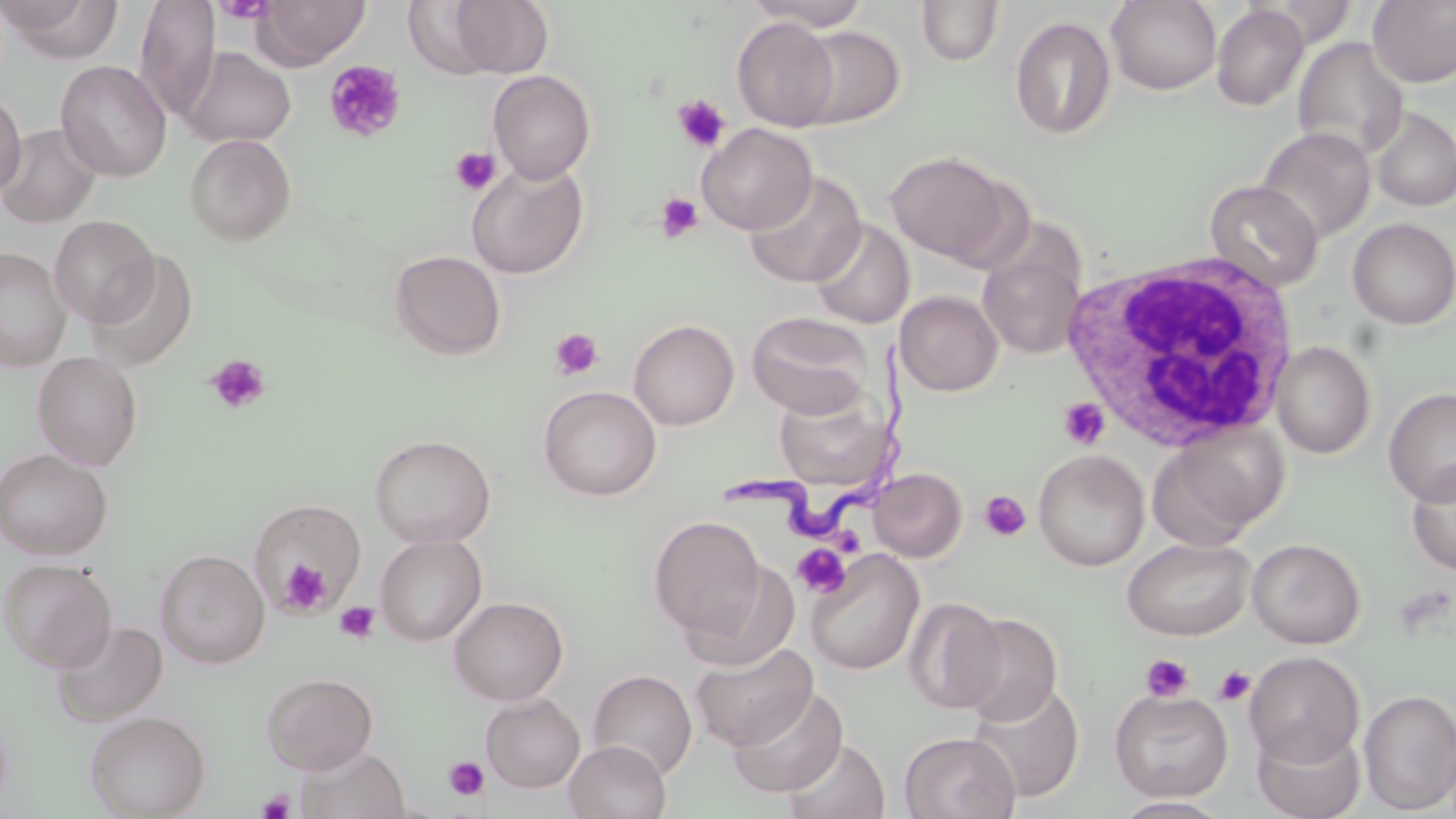
Approximate bounding boxes as (x1,y1)-(x2,y2) corner pairs in pixels. Platelet locations: (216,0)-(275,23), (324,60)-(406,143), (672,94)-(731,153), (449,146)-(501,195), (655,192)-(703,243), (548,328)-(604,381), (205,354)-(272,415), (1058,398)-(1110,450), (980,490)-(1031,541), (792,544)-(851,599), (280,561)-(331,611), (334,600)-(379,644), (1141,654)-(1194,702), (1213,665)-(1256,706), (443,756)-(490,801), (257,788)-(295,818). Trypanosoma brucei locations: (724,337)-(921,545). White blood cell locations: (1062,251)-(1303,454). Uninfected red blood cell locations: (2,0)-(123,61), (134,0)-(220,121), (252,0)-(371,69), (744,0)-(873,31), (1368,0)-(1456,87), (447,1)-(554,76), (916,1)-(1004,66), (1106,1)-(1221,95), (1210,3)-(1309,111), (1009,10)-(1219,118), (1010,16)-(1116,140), (732,17)-(840,131), (791,25)-(905,128), (1292,36)-(1409,161), (180,46)-(296,148), (56,60)-(171,181), (488,70)-(596,183), (0,89)-(26,198), (1371,107)-(1456,211), (0,123)-(101,228), (697,123)-(817,235), (1256,127)-(1376,243), (185,133)-(297,246), (885,151)-(1013,264), (466,160)-(589,279), (745,172)-(866,288), (1204,180)-(1323,292), (49,215)-(159,327), (1347,217)-(1456,329), (808,219)-(914,329), (0,247)-(71,371), (978,248)-(1085,360), (390,250)-(506,360), (84,252)-(199,371), (895,290)-(1003,396), (746,312)-(874,418), (628,318)-(740,430), (1271,340)-(1376,459), (32,350)-(143,470), (538,385)-(661,501), (1383,387)-(1456,505), (773,392)-(892,492), (1148,423)-(1286,549), (368,434)-(496,548), (0,447)-(113,560), (1033,449)-(1149,571), (1406,463)-(1456,576), (869,468)-(967,561), (247,500)-(367,614), (648,514)-(767,639), (375,534)-(487,645), (1121,536)-(1255,641), (1247,538)-(1366,648), (155,549)-(270,669), (805,549)-(924,675), (1,558)-(117,672), (681,560)-(800,672), (448,596)-(568,705), (904,597)-(1007,713), (955,612)-(1063,726), (51,619)-(167,725), (690,642)-(818,751), (1244,651)-(1364,766), (588,669)-(697,780), (262,672)-(378,774), (967,680)-(1085,802), (728,684)-(849,798), (1359,688)-(1456,813), (1109,689)-(1234,801), (481,693)-(584,793), (85,710)-(211,819), (1251,721)-(1365,819), (899,732)-(1020,819), (783,738)-(890,819), (564,739)-(671,819), (295,746)-(411,819), (1109,796)-(1235,818). Slide-level diagnosis: Trypanosoma brucei. Image is 1456×819 pixels. One field of a larger specimen. May-Grünwald-Giemsa stain. Captured at 1000x magnification. Thin blood smear. Optical microscopy.